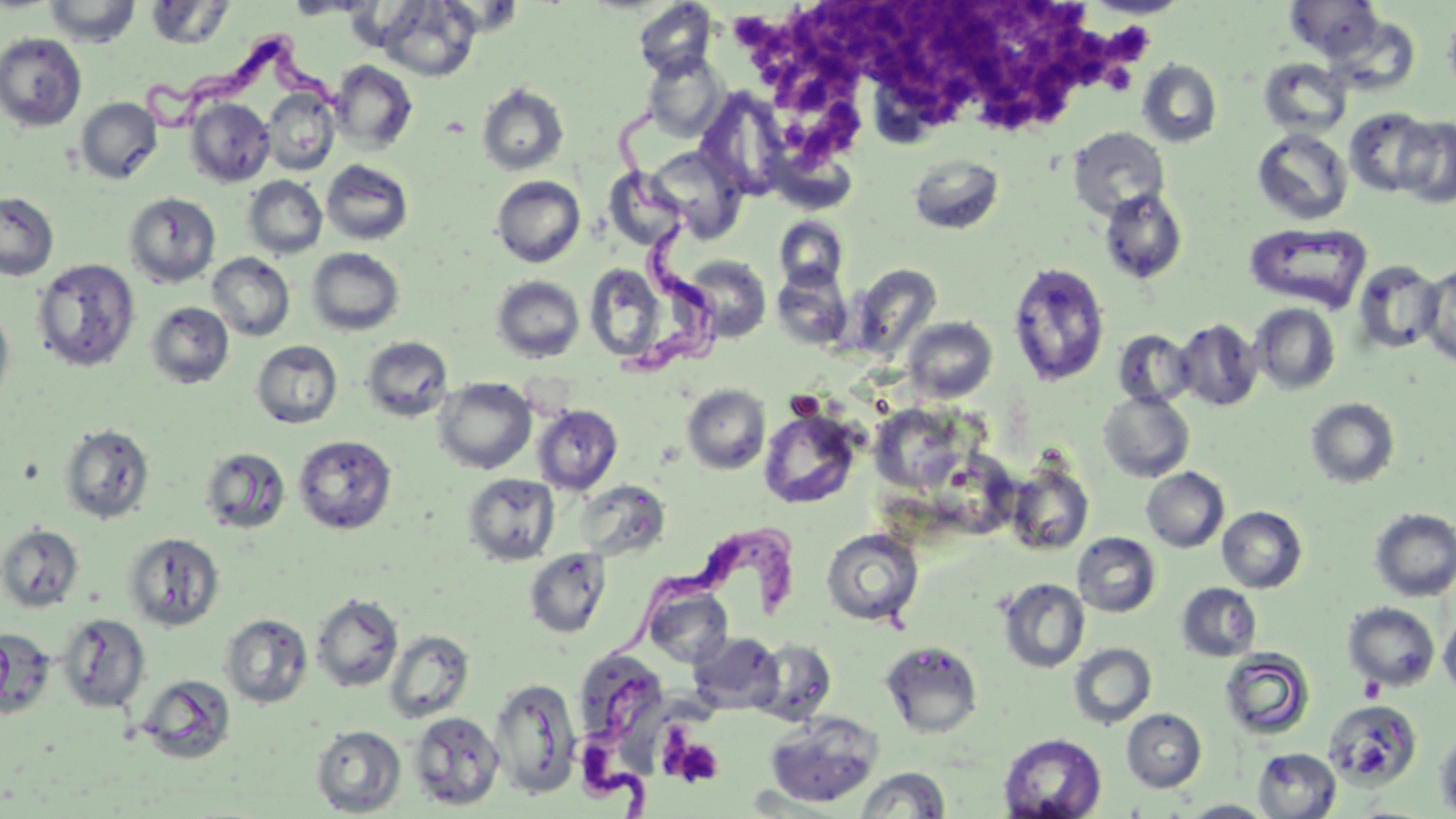
trypanosoma_brucei_locations: 'approximate bounding boxes as (x1, y1, x2, y2) in pixels: (138, 33, 346, 132), (606, 101, 728, 375), (601, 522, 802, 664), (575, 675, 665, 814)'
slide_level_diagnosis: Trypanosoma brucei
uninfected_red_blood_cell_locations: 'approximate bounding boxes as (x1, y1, x2, y2) in pixels: (44, 0, 141, 47), (285, 0, 374, 19), (1082, 0, 1190, 19), (1286, 0, 1383, 61), (145, 1, 234, 49), (377, 1, 480, 82), (633, 1, 717, 80), (1443, 12, 1456, 99), (0, 33, 86, 131), (641, 51, 728, 141), (1259, 58, 1351, 138), (1137, 59, 1222, 147), (328, 60, 418, 154), (476, 83, 569, 176), (262, 88, 339, 175), (695, 88, 790, 199), (75, 97, 162, 184), (186, 98, 275, 186), (1345, 108, 1435, 196), (1393, 117, 1456, 208), (1068, 127, 1170, 219), (1252, 129, 1352, 224), (647, 145, 747, 243), (907, 154, 1005, 235), (321, 159, 414, 246), (604, 168, 687, 250), (244, 176, 327, 259), (492, 176, 585, 267), (1099, 188, 1187, 285), (0, 191, 59, 281), (124, 192, 221, 287), (774, 217, 848, 291), (1245, 223, 1372, 312), (307, 247, 404, 335), (207, 253, 295, 340), (684, 254, 772, 343), (32, 259, 140, 371), (1353, 260, 1441, 355), (1007, 262, 1111, 387), (585, 263, 669, 362), (853, 263, 942, 357), (1416, 263, 1456, 366), (770, 268, 851, 351), (491, 275, 585, 363), (146, 302, 234, 389), (1250, 304, 1340, 395), (0, 305, 16, 409), (903, 316, 998, 402), (1174, 319, 1262, 411), (1113, 329, 1195, 409), (360, 336, 454, 422), (252, 340, 343, 429), (432, 377, 537, 474), (682, 384, 771, 474), (1099, 391, 1194, 481), (1306, 398, 1400, 488), (869, 403, 966, 493), (532, 405, 623, 495), (759, 409, 861, 509), (58, 423, 155, 523), (293, 434, 397, 535), (199, 446, 291, 535), (1006, 460, 1094, 555), (1141, 467, 1229, 552), (463, 473, 560, 565), (575, 480, 670, 561), (1217, 506, 1307, 593), (1370, 508, 1456, 601), (0, 524, 83, 612), (820, 528, 924, 626), (123, 532, 225, 631), (1073, 533, 1161, 617), (524, 548, 612, 637), (998, 578, 1090, 673), (643, 580, 734, 667), (1177, 583, 1261, 661), (311, 593, 403, 692), (1343, 602, 1440, 691), (1439, 609, 1456, 700), (56, 613, 150, 712), (221, 614, 312, 708), (1, 628, 55, 720), (384, 629, 475, 723), (688, 630, 783, 714), (752, 640, 838, 726), (880, 640, 984, 738), (1068, 643, 1157, 728), (1220, 649, 1316, 741), (137, 674, 236, 764), (489, 677, 582, 798), (1323, 698, 1423, 788), (1122, 709, 1206, 792), (407, 711, 505, 810), (764, 712, 882, 807), (311, 725, 406, 817), (1435, 728, 1456, 818), (999, 733, 1106, 819), (1253, 748, 1341, 818), (854, 767, 950, 818), (1181, 800, 1275, 818)'
stain: May-Grünwald-Giemsa
magnification: 1000x
field_of_view: one of a larger specimen
modality: optical microscopy
preparation: thin blood smear
image_size: 1456×819 pixels
platelet_locations: 'approximate bounding boxes as (x1, y1, x2, y2) in pixels: (790, 2, 992, 129), (739, 7, 791, 80), (1109, 22, 1154, 73), (983, 25, 1119, 128), (794, 101, 866, 161), (787, 390, 824, 419), (1359, 675, 1384, 702), (663, 732, 724, 788)'